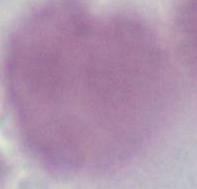

Micrograph. A red blood cell is seen. 1000x magnification.